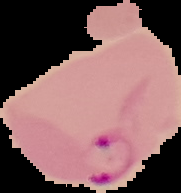
Summary:
  - Image size: 181×193 pixels
  - Image type: cell region segmented out of the field of view; surrounding area masked to black
  - Result: Plasmodium parasites identified
  - Preparation: thin blood film